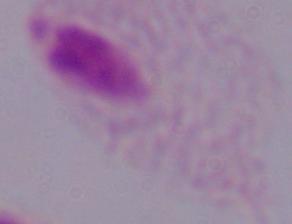
identification: trichomonad
magnification: 1000x
modality: photomicrograph